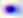

Summary:
  - Magnification: 400x
  - Identification: Toxoplasma gondii
  - Modality: micrograph